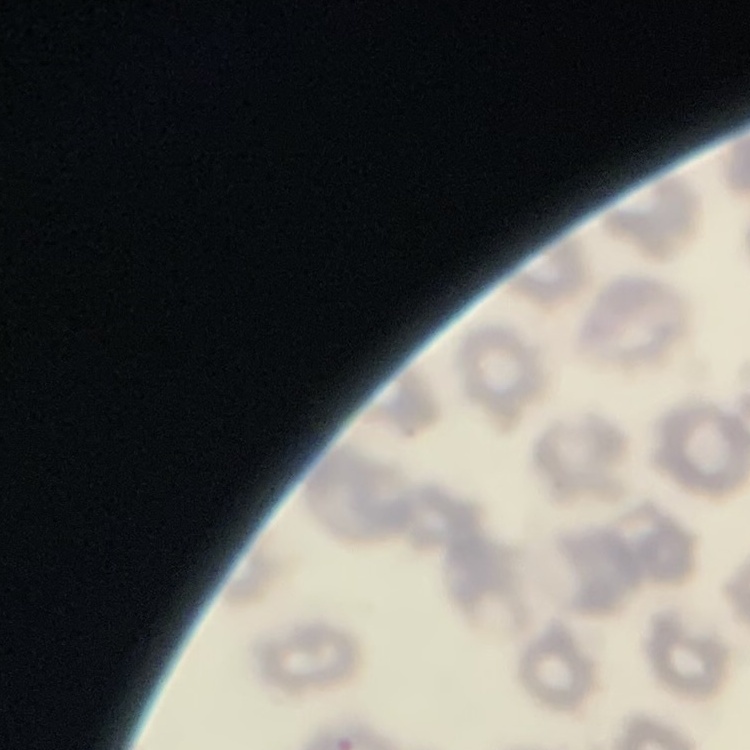 The red blood cells show no rouleaux formation. Square crop of a larger photomicrograph. Stained with either Field's or Giemsa. Thin peripheral smear.